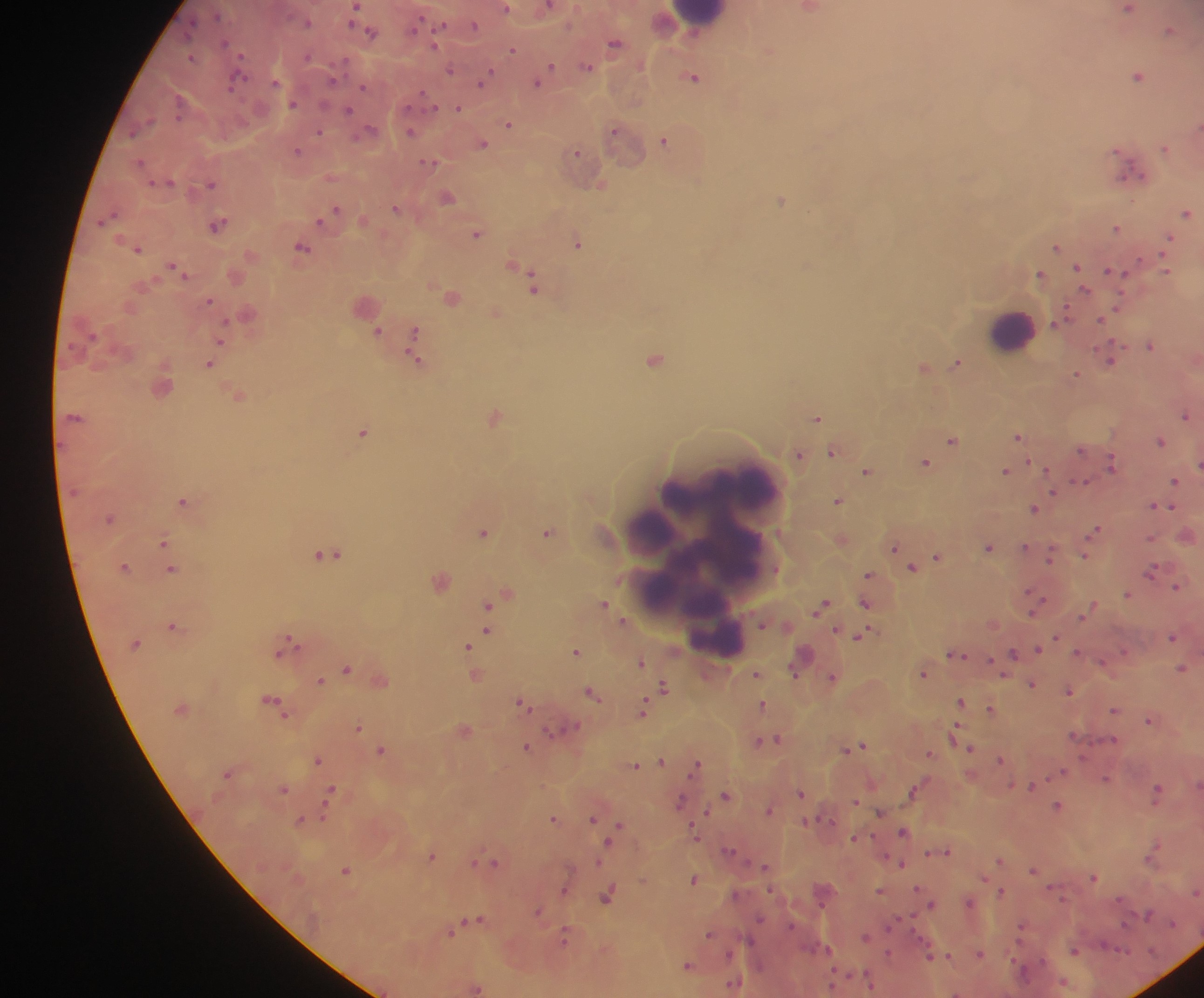
Approximate centers as (x, y) in pixels. Malaria parasite locations: (1128, 8), (808, 9), (369, 29), (1170, 30), (615, 43), (513, 48), (586, 66), (450, 69), (545, 72), (694, 75), (1139, 75), (484, 77), (539, 78), (458, 107), (509, 122), (410, 129), (320, 131), (616, 131), (665, 139), (482, 142), (1165, 147), (298, 150), (576, 154), (430, 161), (1130, 168), (598, 181), (212, 182), (448, 196), (782, 199), (397, 207), (334, 210), (1187, 212), (327, 216), (217, 224), (1117, 227), (478, 232), (1167, 240), (579, 242), (137, 246), (1059, 246), (303, 248), (176, 267), (519, 269), (1114, 270), (1041, 275), (533, 279), (452, 296), (365, 304), (496, 312), (416, 329), (379, 331), (220, 339), (1151, 343), (414, 344), (418, 357), (655, 357), (1111, 357), (958, 361), (209, 362), (925, 366), (1077, 374), (238, 393), (1186, 413), (496, 416), (817, 417), (363, 432), (1019, 434), (953, 439), (1161, 439), (834, 451), (800, 453), (926, 461), (1113, 461), (1197, 464), (868, 470), (1006, 470), (1084, 481), (1176, 481), (1053, 492), (839, 499), (185, 500), (1158, 505), (1035, 507), (1095, 530), (548, 531), (484, 532), (1187, 533), (1151, 537), (165, 539), (842, 539), (989, 546), (897, 547), (330, 553), (1051, 553), (1087, 553), (938, 555), (907, 559), (124, 565), (913, 565), (172, 568), (1152, 570), (870, 574), (440, 579), (1178, 584), (507, 592), (1128, 592), (1035, 599), (866, 600), (488, 603), (604, 603), (823, 603), (1093, 605), (1085, 614), (624, 619), (762, 623), (174, 625), (488, 629), (862, 633), (1173, 635), (1057, 636), (289, 644), (468, 646), (1038, 647), (577, 651), (1078, 652), (957, 653), (1013, 653), (802, 657), (641, 660), (348, 667), (797, 667), (1183, 668), (924, 672), (757, 674), (477, 675), (833, 676), (380, 678), (322, 680), (1033, 683), (665, 686), (1069, 689), (593, 693), (962, 701), (275, 702), (523, 702), (763, 705), (991, 708), (644, 709), (1115, 709), (1150, 718), (358, 727), (465, 728), (565, 729), (957, 735), (1074, 735), (774, 738), (762, 741), (860, 745), (527, 746), (970, 747), (848, 748), (382, 749), (930, 752), (1001, 758), (318, 759), (661, 759), (636, 764), (697, 764), (1063, 771), (1106, 778), (1033, 785), (283, 788), (915, 789), (332, 791), (1158, 791), (801, 792), (726, 794), (680, 801), (856, 801), (1058, 804), (326, 808), (769, 808), (706, 812), (881, 812), (555, 818), (594, 818), (301, 819), (807, 821), (619, 824), (903, 831), (696, 834), (855, 837), (612, 839), (729, 851), (947, 851), (1154, 851), (930, 853), (433, 855), (999, 860), (477, 861), (494, 861), (901, 863), (765, 865), (347, 869), (1034, 870), (1094, 877), (695, 879), (919, 888), (565, 889), (880, 890), (1001, 891), (1196, 893), (608, 895), (970, 902), (931, 903), (538, 911), (475, 919), (468, 924), (451, 931), (710, 934), (566, 936), (866, 936), (1074, 951), (889, 953), (980, 953), (948, 955), (930, 956), (689, 965), (870, 981), (735, 984), (832, 984), (476, 987), (956, 992). Leukocyte locations: (700, 18), (1014, 329), (731, 489), (702, 552), (714, 555). Photographed through a microscope with a mobile-phone camera. Image is 1204×998 pixels. Thick blood smear. One field of view. Collected in Ghana.